Locate and identify every blood parasite.
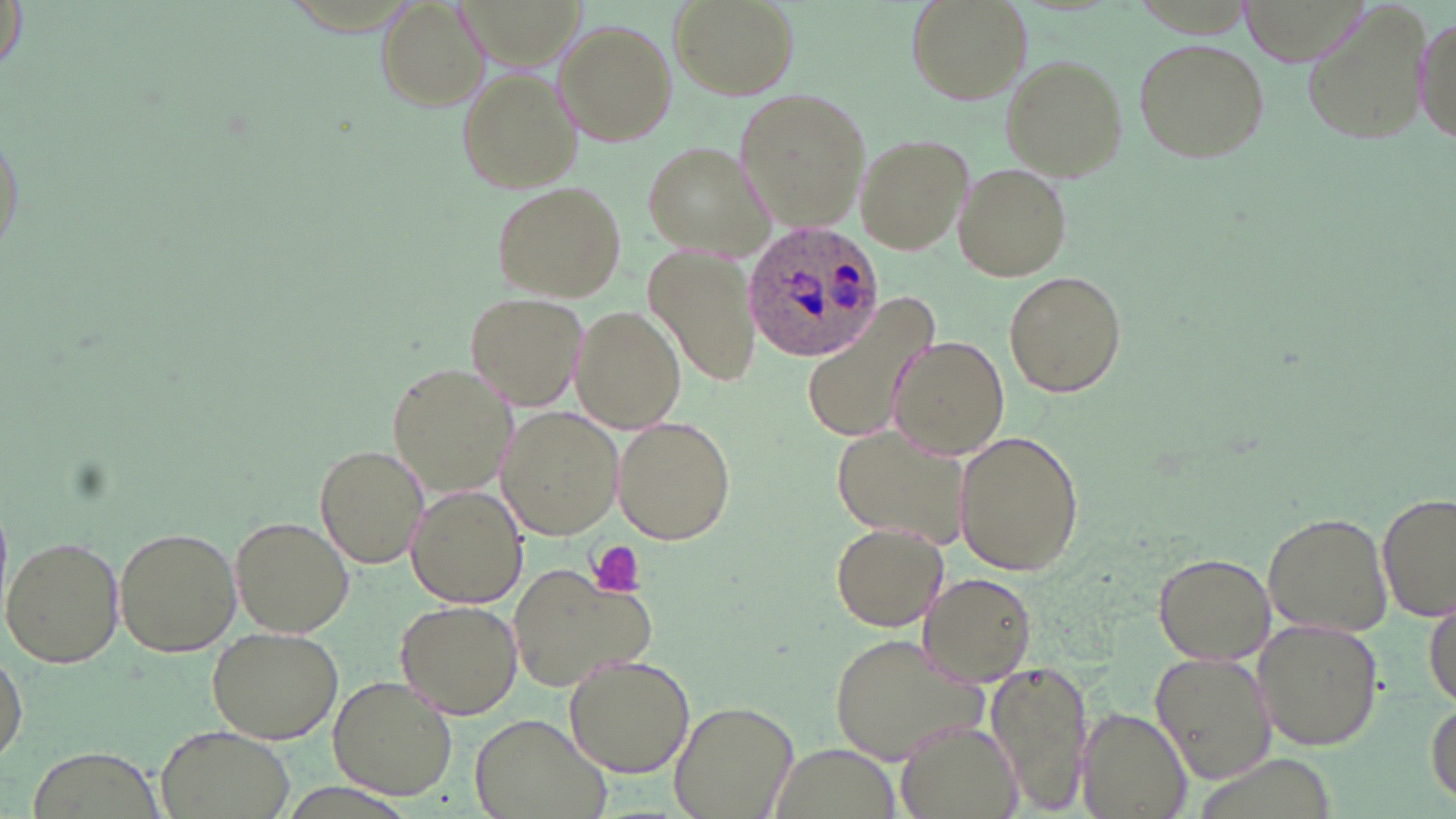
Approximate bounding boxes as [x1, y1, x2, y2] in pixels.
Plasmodium ovale-infected red blood cells: [741, 220, 892, 361].
No Plasmodium falciparum, Plasmodium malariae, Plasmodium vivax, Babesia divergens, or Trypanosoma brucei observed.

Platelet locations: [586, 542, 646, 598]. Uninfected red blood cell locations: [669, 0, 799, 100], [904, 0, 1034, 107], [1302, 0, 1430, 150], [373, 1, 489, 113], [1414, 7, 1452, 160], [554, 19, 677, 145], [1133, 36, 1270, 165], [1000, 55, 1128, 181], [457, 70, 579, 192], [736, 88, 872, 231], [854, 134, 971, 254], [640, 140, 773, 259], [951, 160, 1070, 281], [491, 179, 627, 301], [644, 248, 760, 390], [1003, 271, 1127, 398], [466, 290, 588, 410], [799, 295, 940, 451], [571, 306, 688, 433], [891, 334, 1012, 460], [389, 360, 513, 495], [499, 405, 625, 539], [611, 417, 735, 545], [830, 424, 974, 549], [953, 429, 1084, 577], [315, 444, 428, 571], [406, 485, 526, 607], [1377, 491, 1454, 623], [1263, 510, 1393, 639], [230, 515, 354, 640], [830, 524, 948, 632], [113, 525, 241, 656], [4, 535, 124, 668], [1153, 552, 1277, 665], [507, 560, 660, 694], [916, 570, 1037, 687], [1426, 592, 1456, 712], [397, 599, 522, 717], [1253, 620, 1386, 750], [205, 628, 342, 742], [827, 632, 990, 765], [1, 644, 26, 763], [1149, 651, 1278, 786], [564, 653, 695, 777], [987, 659, 1095, 812], [328, 674, 457, 801], [1426, 697, 1455, 807], [670, 698, 802, 819], [1075, 708, 1191, 819], [469, 713, 609, 819], [895, 719, 1022, 819], [154, 725, 298, 819]. Slide-level diagnosis: Plasmodium ovale. Optical microscopy. 1000x magnification. One field of a larger specimen. Thin blood smear. Image is 1456×819 pixels. May-Grünwald-Giemsa-stained preparation.